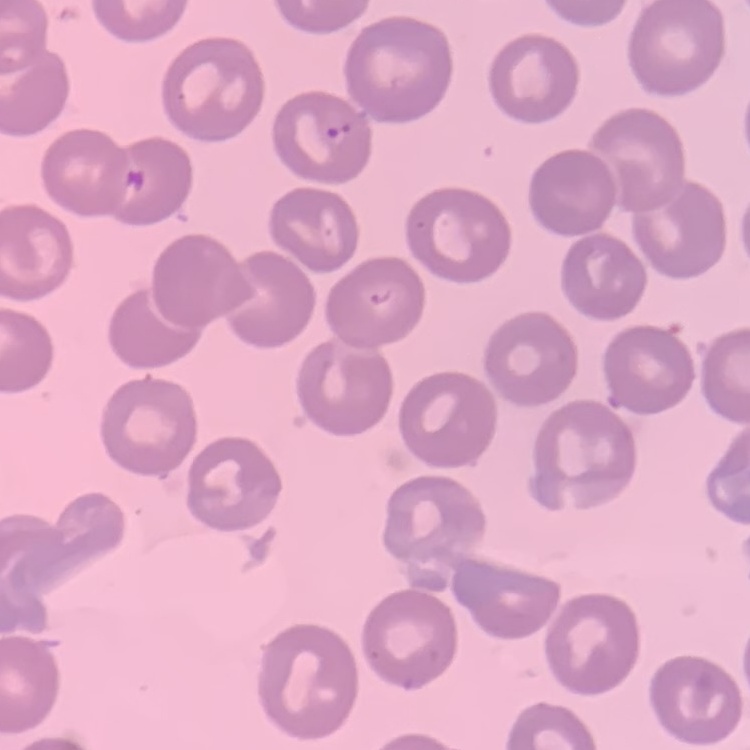 The red blood cells exhibit no rouleaux formation. Square crop of a larger photomicrograph. Thin peripheral smear. Field's or Giemsa stain.